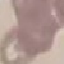
Summary:
  - Malaria status: uninfected
  - Image type: cell patch, automatically extracted from a larger field of view and resized to 64 × 64 pixels
  - Capture: smartphone camera at the microscope eyepiece
  - Preparation: thin smear
  - Stain: Giemsa